Outline each blood parasite and name the species.
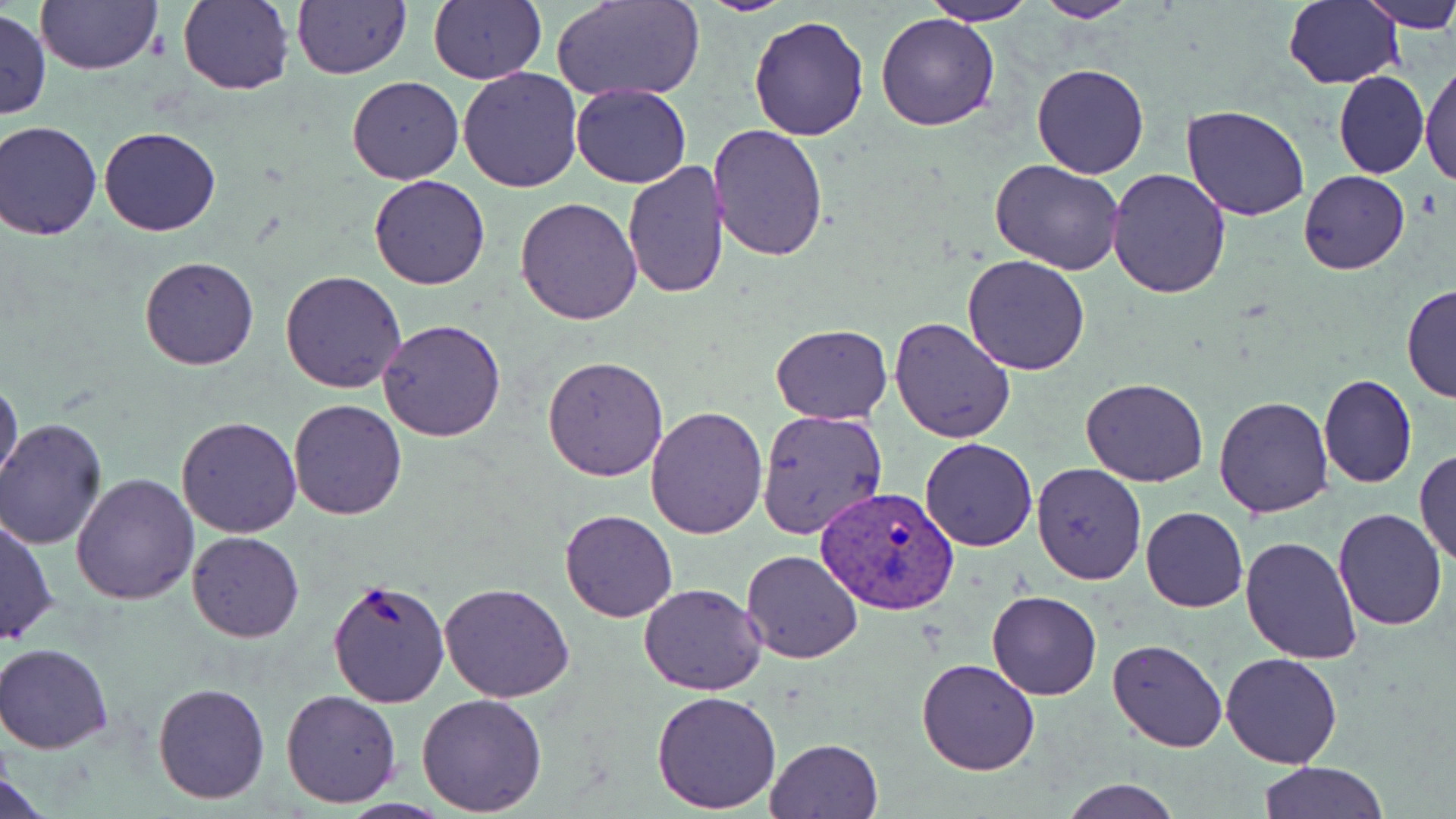
Approximate bounding boxes as (x1, y1, x2, y2) in pixels.
Plasmodium vivax-infected red blood cells: (813, 486, 958, 615).
No Plasmodium falciparum, Plasmodium ovale, Plasmodium malariae, Babesia divergens, or Trypanosoma brucei observed.

slide-level diagnosis = Plasmodium vivax
uninfected red blood cell locations = approximate bounding boxes as (x1, y1, x2, y2) in pixels: (34, 0, 164, 75), (176, 0, 294, 93), (293, 0, 410, 79), (427, 0, 545, 84), (555, 0, 703, 102), (688, 0, 800, 15), (922, 0, 1036, 25), (1033, 0, 1138, 23), (1282, 0, 1403, 89), (1358, 0, 1456, 33), (1, 9, 51, 121), (875, 11, 999, 131), (748, 13, 870, 140), (1419, 55, 1455, 189), (1030, 63, 1151, 180), (458, 67, 583, 193), (1333, 70, 1428, 179), (1318, 71, 1420, 278), (346, 76, 465, 185), (569, 83, 691, 188), (1181, 104, 1312, 221), (1, 121, 103, 240), (707, 124, 828, 262), (99, 126, 220, 236), (991, 160, 1126, 277), (622, 161, 730, 299), (1106, 166, 1232, 298), (1298, 170, 1410, 275), (370, 176, 490, 291), (514, 196, 642, 324), (962, 254, 1090, 375), (138, 255, 260, 371), (279, 270, 407, 393), (1402, 284, 1456, 403), (889, 316, 1017, 443), (377, 318, 508, 442), (769, 323, 892, 423), (542, 355, 670, 481), (0, 372, 24, 492), (1318, 374, 1417, 490), (1081, 378, 1208, 488), (1213, 394, 1333, 517), (287, 398, 409, 520), (646, 406, 768, 540), (756, 407, 889, 541), (176, 415, 304, 537), (1, 418, 107, 548), (919, 438, 1037, 551), (1415, 449, 1456, 567), (1030, 463, 1148, 586), (72, 474, 200, 607), (1142, 507, 1248, 613), (1334, 507, 1448, 629), (558, 510, 678, 623), (1, 516, 57, 646), (186, 531, 304, 643), (1239, 536, 1362, 664), (739, 549, 865, 664), (327, 577, 448, 708), (439, 583, 574, 702), (638, 583, 766, 695), (986, 588, 1102, 701), (1108, 640, 1228, 753), (0, 642, 113, 754), (1221, 652, 1343, 768), (916, 656, 1041, 775), (152, 681, 272, 804), (282, 689, 400, 807), (651, 690, 782, 812), (416, 692, 548, 814), (768, 738, 883, 818), (1259, 760, 1388, 819), (0, 770, 54, 818), (1058, 778, 1184, 818)
modality = light microscopy
preparation = thin blood smear
field of view = single
stain = May-Grünwald-Giemsa
image size = 1456×819 pixels
magnification = 1000x